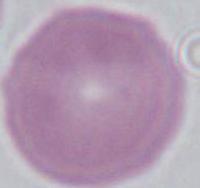
identification = red blood cell
magnification = 1000x
modality = micrograph